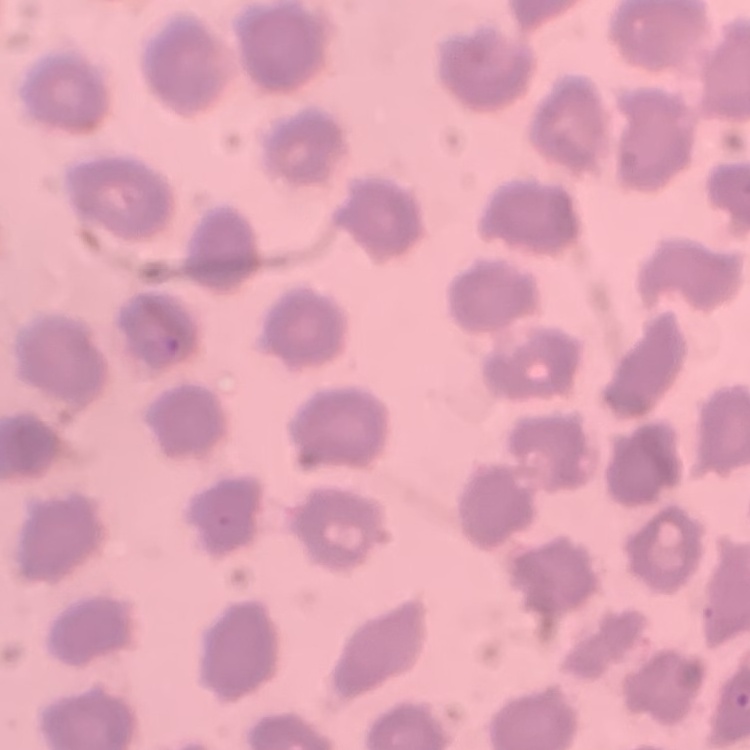

red_blood_cell_morphology: no rouleaux formation
stain: Field's or Giemsa
preparation: thin peripheral smear
image_type: one tile cut from a larger photomicrograph